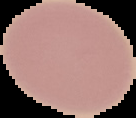
Summary:
  - Result: negative for Plasmodium parasites
  - Preparation: thin blood film
  - Image type: segmented cell region with the area outside set to black
  - Image size: 136×118 pixels